Assess for parasitized red blood cells.
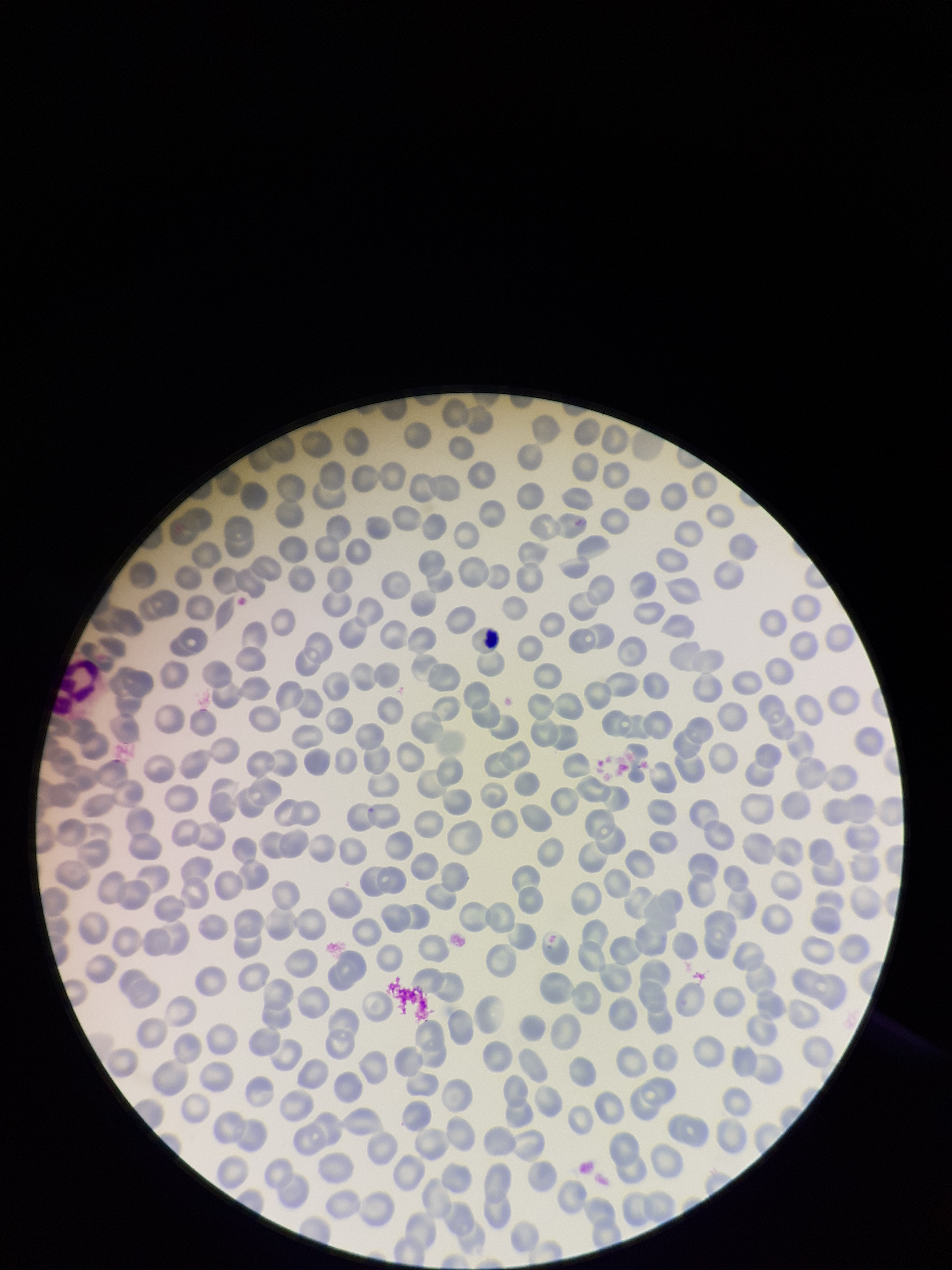

None identified.

patient malaria status = negative
stain = Giemsa
capture = smartphone photograph through the microscope eyepiece
parasitized red blood cell count = 0
red blood cell count = 305
image size = 952×1270 pixels
preparation = thin smear
field of view = single